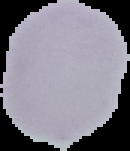
{
  "image_size": "130×151 pixels",
  "preparation": "thin blood smear",
  "result": "negative for Plasmodium parasites",
  "image_type": "segmented cell region on a black background"
}